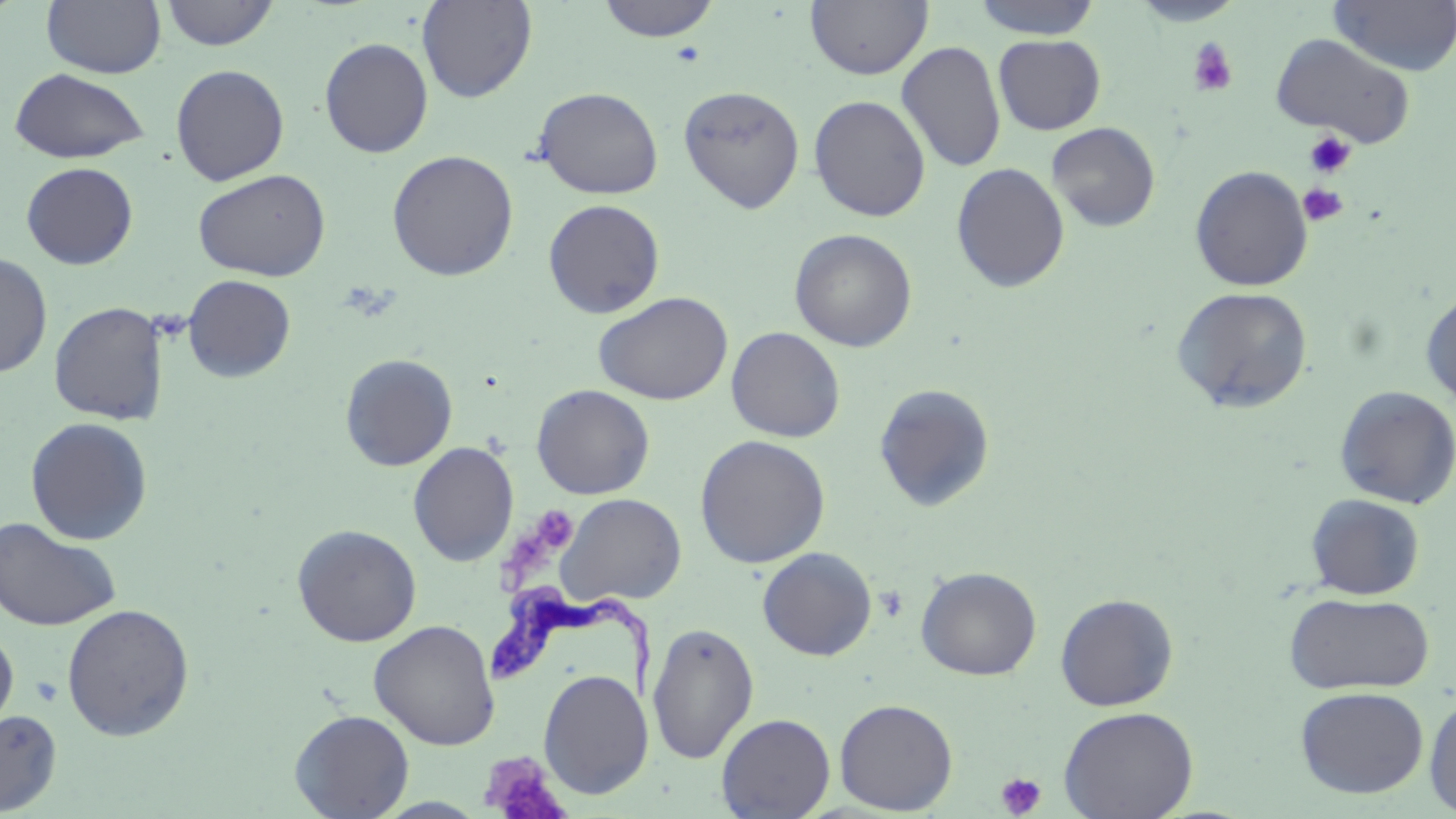

Summary:
  - Coordinate format: approximate bounding boxes as (x1, y1, x2, y2) in pixels
  - Platelet locations: (1187, 37, 1238, 97), (1303, 131, 1354, 179), (1299, 183, 1348, 226), (529, 503, 575, 554), (479, 752, 570, 819), (995, 772, 1047, 818)
  - Trypanosoma brucei locations: (486, 583, 662, 706)
  - Uninfected red blood cell locations: (42, 0, 166, 79), (161, 0, 280, 51), (416, 0, 538, 103), (596, 0, 721, 43), (805, 0, 933, 80), (970, 0, 1104, 39), (1329, 0, 1456, 77), (1129, 1, 1246, 27), (1270, 33, 1417, 148), (993, 34, 1106, 135), (319, 37, 433, 158), (897, 40, 1006, 173), (171, 64, 290, 185), (9, 68, 151, 164), (678, 85, 805, 214), (532, 86, 664, 200), (809, 95, 931, 221), (1046, 121, 1161, 233), (386, 149, 519, 281), (21, 162, 138, 269), (951, 162, 1070, 293), (1190, 165, 1313, 292), (193, 169, 331, 282), (543, 198, 666, 319), (789, 228, 917, 352), (0, 252, 53, 379), (182, 274, 296, 383), (1172, 286, 1313, 414), (1420, 287, 1456, 409), (594, 291, 733, 405), (48, 301, 169, 425), (726, 326, 845, 443), (339, 353, 458, 471), (874, 383, 995, 512), (532, 384, 655, 500), (1334, 385, 1456, 509), (25, 417, 153, 545), (695, 435, 830, 568), (407, 441, 519, 566), (557, 493, 686, 607), (1305, 493, 1425, 600), (0, 516, 121, 632), (292, 523, 422, 646), (757, 547, 877, 661), (916, 566, 1042, 680), (1284, 592, 1435, 695), (1054, 593, 1179, 711), (60, 602, 195, 742), (369, 619, 500, 750), (647, 621, 760, 764), (0, 626, 18, 734), (538, 668, 653, 799), (1295, 686, 1429, 798), (1423, 692, 1456, 816), (834, 698, 958, 815), (1058, 706, 1199, 819), (0, 709, 62, 816), (289, 709, 414, 818), (716, 713, 836, 818), (373, 797, 490, 817)
  - Slide-level diagnosis: Trypanosoma brucei
  - Magnification: 1000x
  - Preparation: thin blood smear
  - Stain: May-Grünwald-Giemsa
  - Modality: optical microscopy
  - Field of view: single
  - Image size: 1456×819 pixels